State which parasite is depicted.
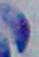

Toxoplasma gondii.

Summary:
  - Magnification: 1000x
  - Modality: micrograph